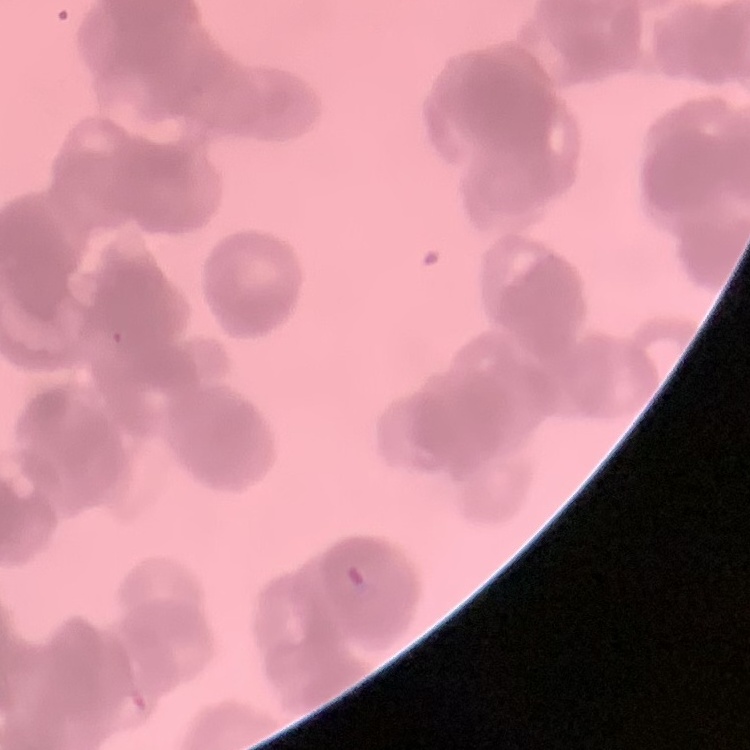
The red blood cells show rouleaux formation. One tile cut from a larger photomicrograph. Thin blood film. Stained with either Field's or Giemsa.